Report the malaria status of this cell.
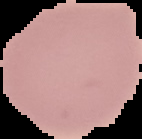
It is uninfected.

Summary:
  - Preparation: thin blood film
  - Image size: 142×139 pixels
  - Image type: cell region segmented out of the field of view; surrounding area masked to black